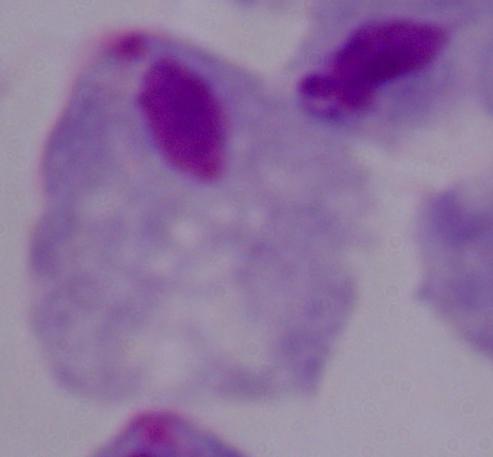

{
  "magnification": "1000x",
  "identification": "trichomonad",
  "modality": "micrograph"
}